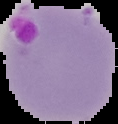

{
  "preparation": "thin blood smear",
  "image_type": "cell region segmented out of the field of view; surrounding area masked to black",
  "image_size": "118×124 pixels",
  "malaria_status": "parasitized"
}